Evaluate for malaria.
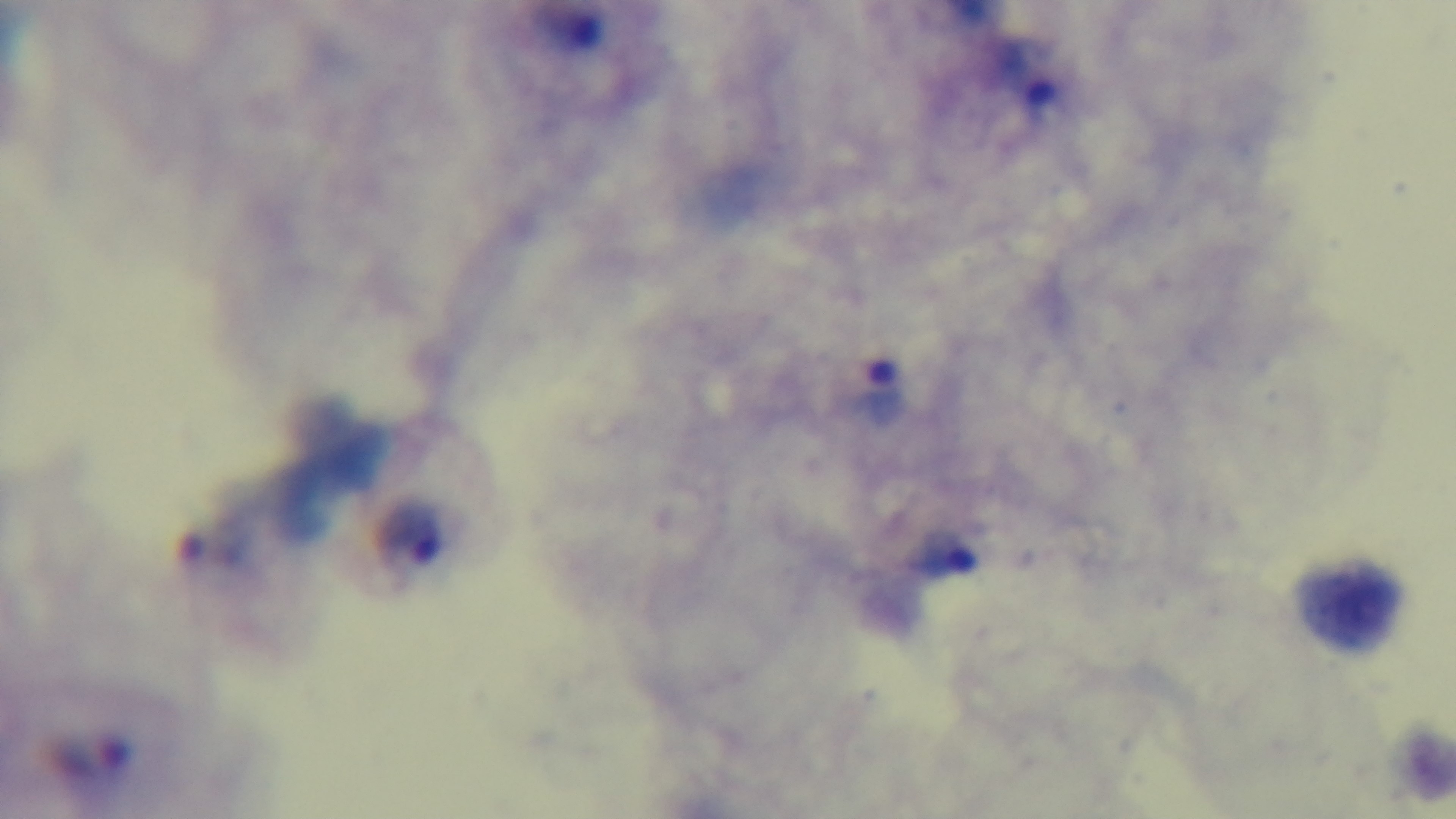

It is infected.

Summary:
  - Field of view: single
  - Objective: 100x oil immersion
  - Capture: mounted 4K digital camera
  - Modality: light microscopy
  - Preparation: thick smear
  - Stain: Giemsa